Report the malaria status of this cell.
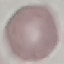
Uninfected.

Summary:
  - Capture: smartphone through the microscope eyepiece
  - Stain: Giemsa
  - Image type: cell patch, automatically extracted from a larger field of view and resized to 64 × 64 pixels
  - Preparation: thin smear